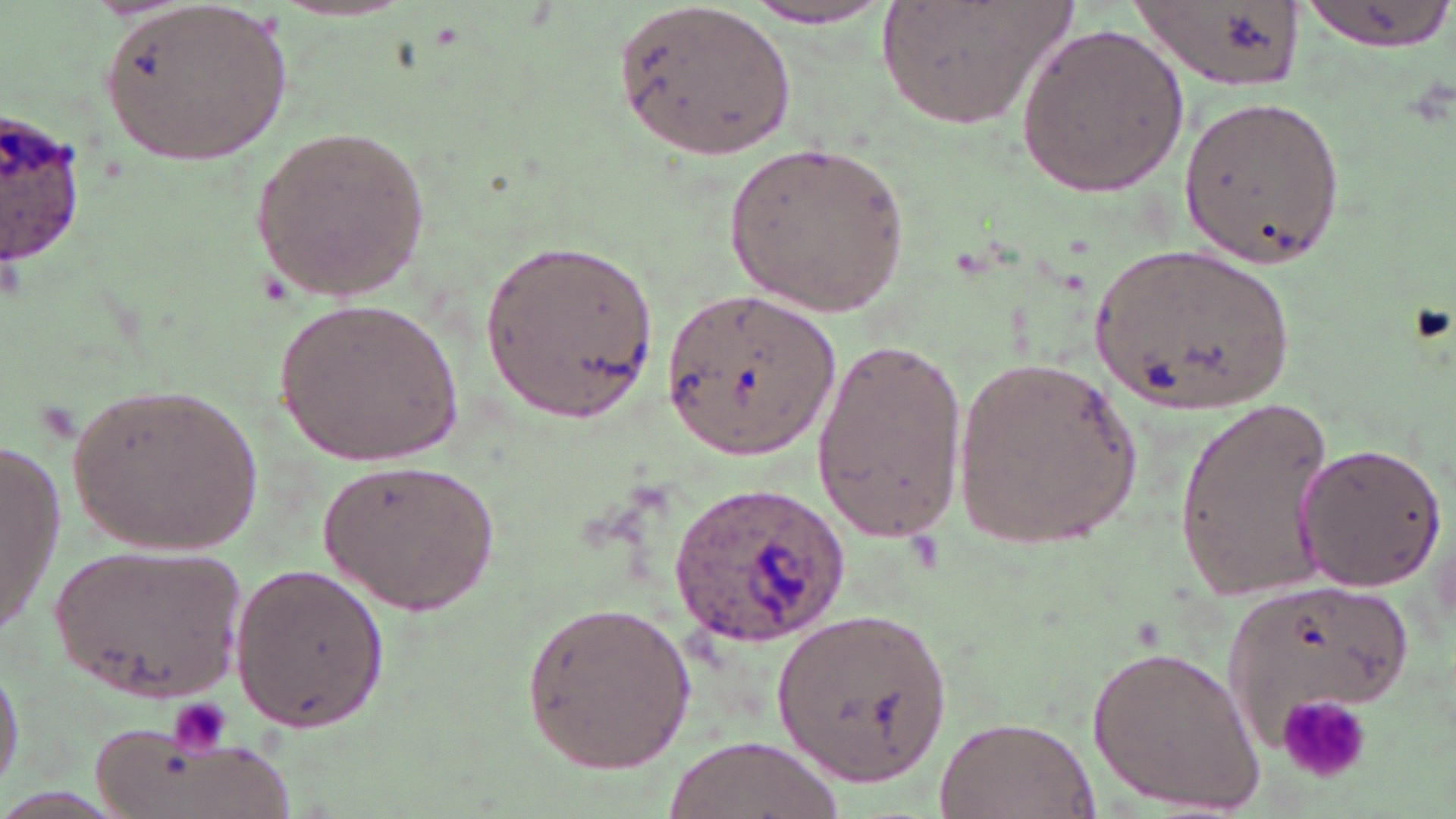

Summary:
  - Coordinate format: approximate bounding boxes as [x1, y1, x2, y2] in pixels
  - Plasmodium ovale-infected red blood cell locations: [1, 116, 91, 270], [669, 483, 852, 647]
  - Platelet locations: [1275, 689, 1376, 784], [166, 699, 229, 757]
  - Uninfected red blood cell locations: [872, 0, 1082, 131], [1296, 0, 1452, 51], [99, 1, 295, 165], [613, 2, 797, 160], [737, 2, 897, 29], [1130, 2, 1306, 91], [1016, 22, 1192, 198], [1178, 94, 1347, 271], [249, 123, 435, 306], [722, 142, 912, 320], [482, 241, 665, 419], [1090, 244, 1299, 416], [663, 283, 842, 461], [275, 296, 466, 466], [806, 334, 965, 538], [954, 352, 1146, 554], [60, 380, 269, 560], [1170, 393, 1335, 603], [0, 441, 66, 634], [1295, 441, 1446, 592], [317, 457, 501, 618], [49, 542, 248, 704], [229, 564, 389, 734], [1221, 585, 1412, 757], [516, 597, 700, 775], [777, 607, 957, 785], [1088, 642, 1269, 814], [0, 651, 22, 797], [934, 715, 1101, 818], [92, 725, 293, 819], [664, 735, 835, 819]
  - Slide-level diagnosis: Plasmodium ovale
  - Magnification: 1000x
  - Field of view: one of a larger specimen
  - Modality: light microscopy
  - Image size: 1456×819 pixels
  - Stain: May-Grünwald-Giemsa
  - Preparation: thin blood film